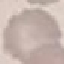 Malaria status: uninfected. Automatically extracted cell patch, resized to 64 × 64 pixels. Thin blood smear. Giemsa stain. Photographed with a smartphone camera at the microscope eyepiece.